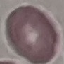
Summary:
  - Result: no malaria parasites seen
  - Stain: Giemsa
  - Image type: automatically extracted cell patch, resized to 64 × 64 pixels
  - Preparation: thin smear
  - Capture: smartphone camera at the microscope eyepiece